Comment on the morphology of the erythrocytes.
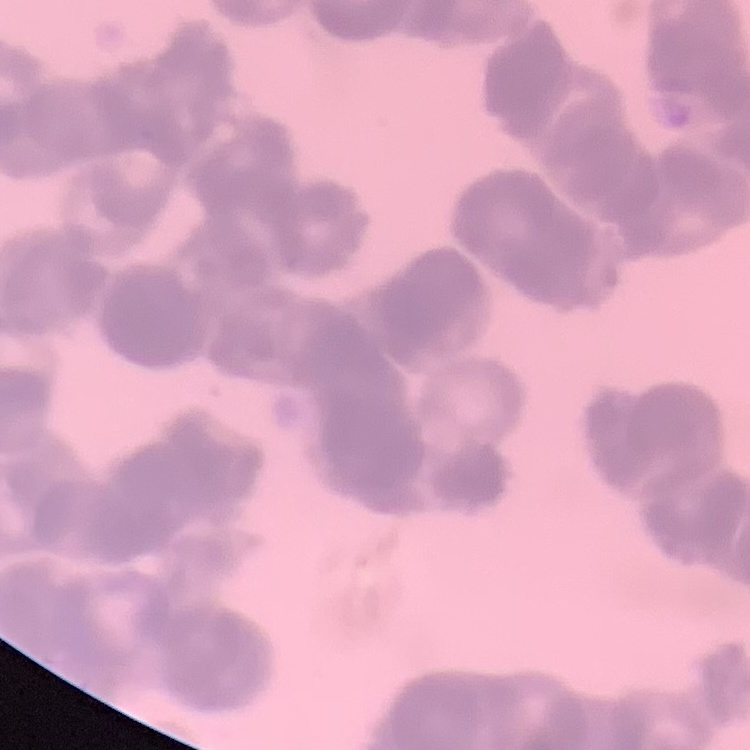

They show rouleaux formation.

preparation = thin blood film
stain = Field's or Giemsa
image type = one tile cut from a larger photomicrograph